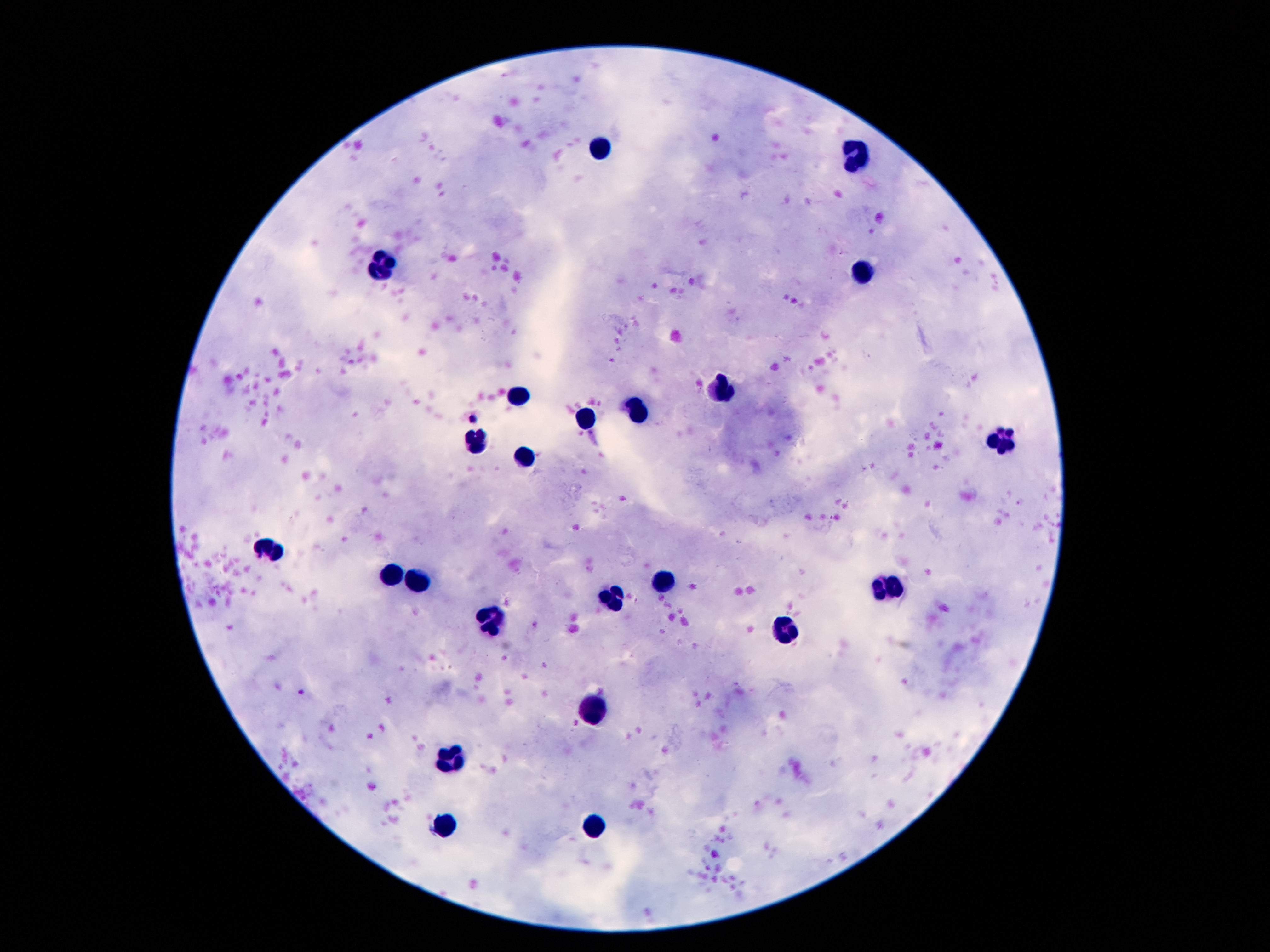

image size = 1270×952 pixels
stain = Giemsa
patient malaria status = uninfected
preparation = thick blood smear
magnification = 100x
field of view = one from this slide
capture = smartphone camera through the microscope eyepiece
leukocyte locations = approximate object centers, in pixels from the top-left corner: (x=602, y=148), (x=858, y=156), (x=383, y=269), (x=863, y=269), (x=724, y=389), (x=514, y=393), (x=640, y=411), (x=586, y=419), (x=1002, y=437), (x=472, y=442), (x=527, y=456), (x=270, y=546), (x=388, y=577), (x=666, y=581), (x=419, y=583), (x=889, y=588), (x=615, y=599), (x=492, y=621), (x=785, y=632), (x=593, y=703), (x=449, y=753), (x=445, y=823), (x=597, y=824)